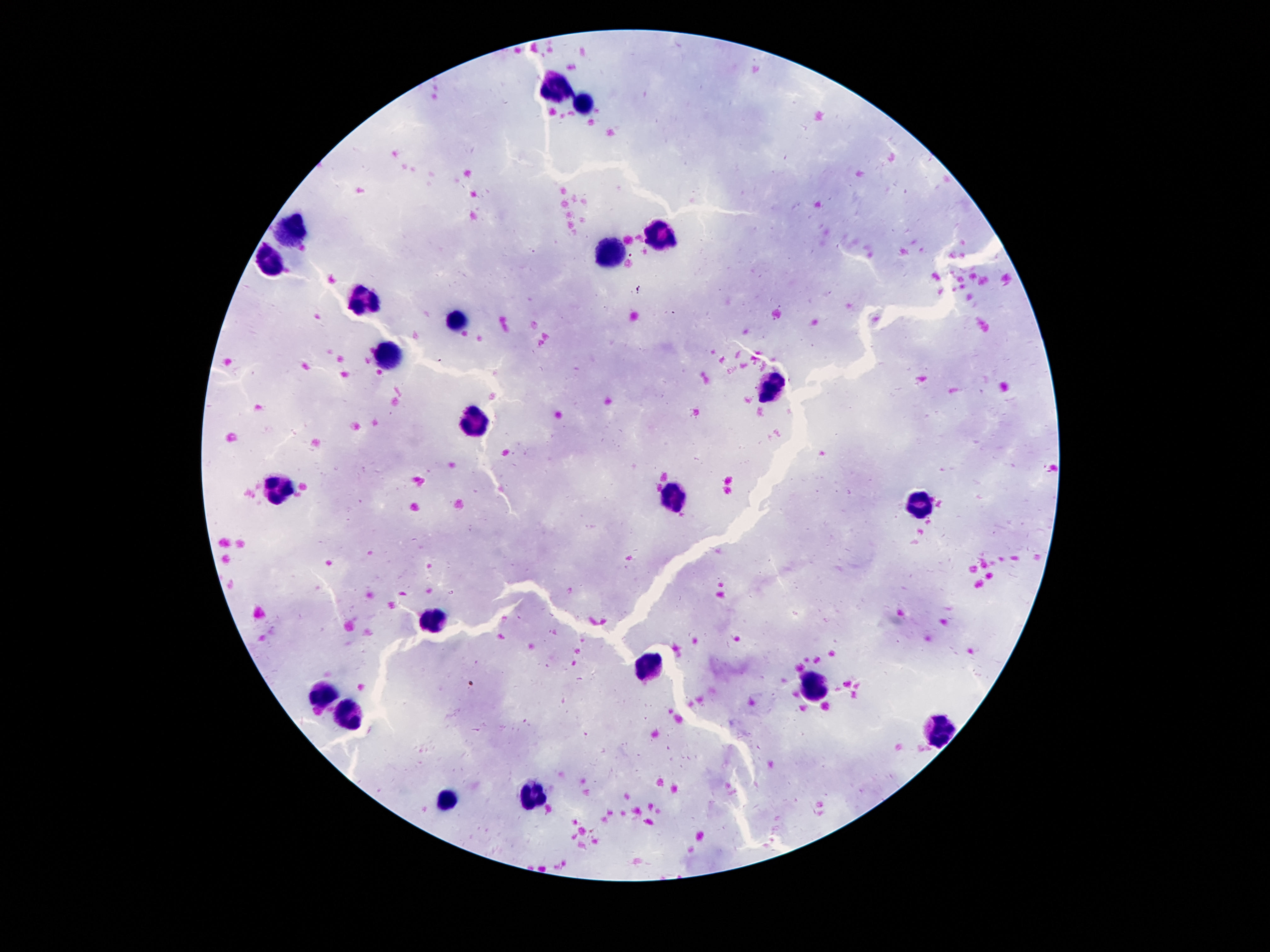
leukocyte_locations: 'approximate object centers, in pixels from the top-left corner: (x=557, y=85), (x=587, y=103), (x=289, y=233), (x=659, y=235), (x=607, y=253), (x=267, y=265), (x=363, y=307), (x=455, y=315), (x=387, y=357), (x=771, y=389), (x=473, y=421), (x=281, y=489), (x=673, y=499), (x=919, y=503), (x=431, y=621), (x=647, y=670), (x=813, y=687), (x=321, y=696), (x=347, y=710), (x=937, y=731), (x=535, y=796), (x=445, y=800)'
preparation: thick peripheral-blood smear
image_size: 1270×952 pixels
capture: smartphone camera through the microscope eyepiece
stain: Giemsa
magnification: 100x
field_of_view: single
patient_malaria_status: negative